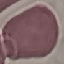 Malaria status: uninfected. Thin blood smear. Acquired by smartphone through the microscope eyepiece. Giemsa-stained preparation. Cell patch, automatically extracted from a larger field of view and resized to 64 × 64 pixels.